Identify the parasite.
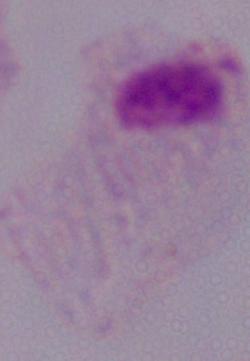

A trichomonad.

Micrograph. Captured at 1000x magnification.